State the blood parasite species.
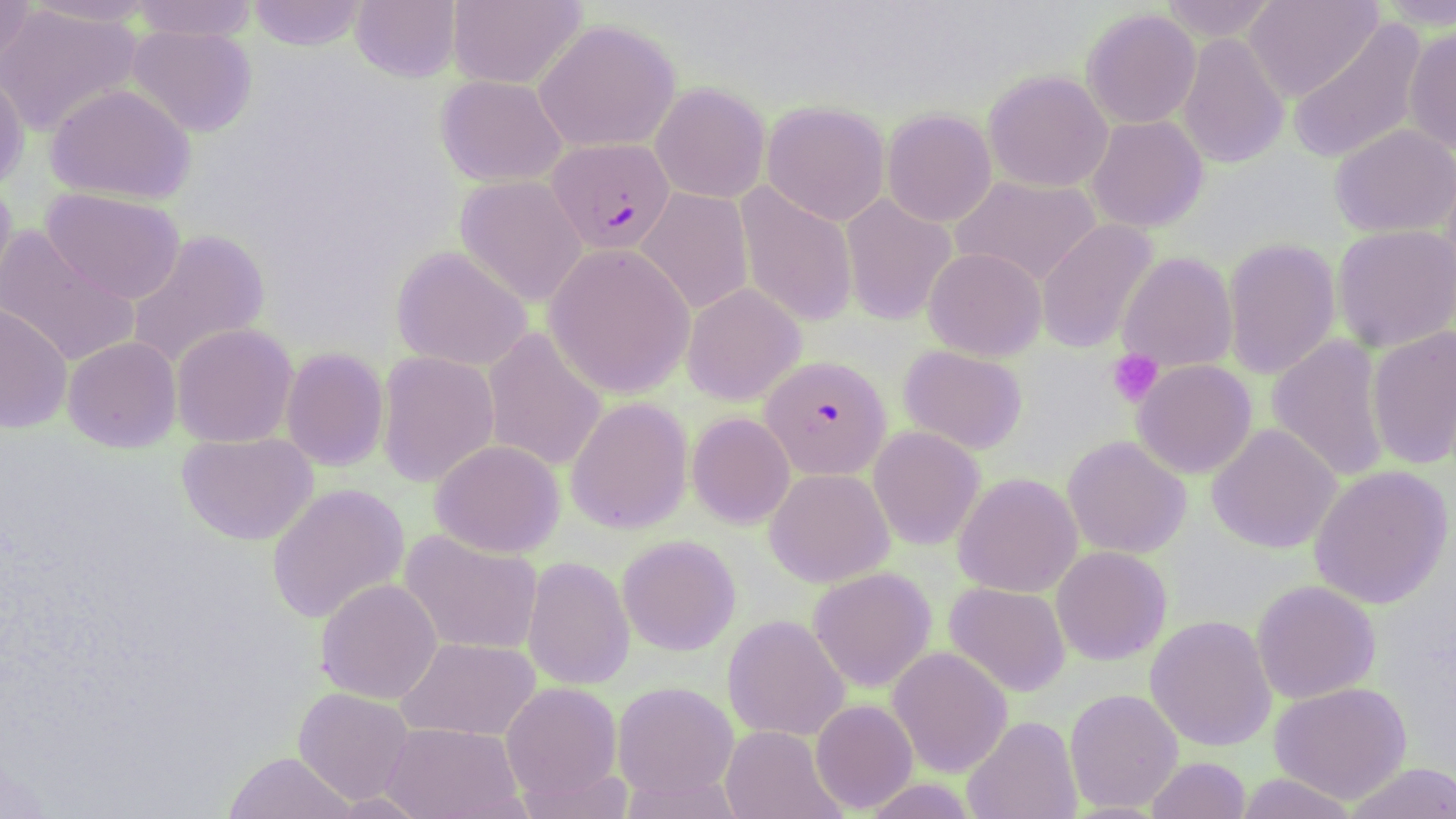
Plasmodium falciparum.

Approximate bounding boxes as [x1, y1, x2, y2] in pixels. Uninfected red blood cell locations: [0, 0, 35, 75], [22, 0, 161, 26], [130, 0, 258, 41], [248, 0, 367, 50], [351, 0, 461, 82], [447, 0, 586, 89], [1158, 0, 1280, 41], [1242, 0, 1381, 101], [1374, 0, 1456, 31], [0, 4, 143, 137], [1081, 7, 1201, 129], [1288, 17, 1428, 165], [533, 18, 681, 153], [126, 24, 258, 137], [1403, 26, 1456, 155], [1176, 32, 1290, 169], [0, 68, 29, 191], [983, 70, 1113, 192], [435, 75, 567, 187], [650, 82, 770, 203], [45, 83, 196, 204], [761, 100, 890, 226], [882, 109, 997, 227], [1086, 115, 1208, 233], [1330, 124, 1456, 238], [1439, 167, 1456, 298], [455, 175, 588, 307], [950, 175, 1102, 287], [0, 176, 17, 306], [734, 183, 859, 328], [41, 188, 186, 304], [635, 188, 754, 315], [840, 194, 957, 326], [1036, 219, 1158, 354], [1332, 224, 1456, 353], [0, 225, 141, 368], [125, 229, 270, 369], [1222, 237, 1341, 380], [544, 243, 695, 399], [391, 246, 533, 372], [923, 247, 1046, 361], [1118, 252, 1237, 372], [682, 283, 806, 406], [0, 302, 72, 434], [171, 323, 298, 448], [1366, 326, 1456, 470], [482, 327, 608, 472], [1267, 335, 1391, 482], [63, 336, 182, 453], [898, 345, 1028, 455], [280, 347, 390, 471], [376, 351, 500, 487], [1132, 359, 1257, 479], [565, 397, 693, 534], [687, 412, 795, 528], [1206, 423, 1342, 554], [867, 425, 985, 551], [177, 431, 318, 545], [1062, 435, 1191, 558], [430, 440, 565, 558], [1308, 465, 1454, 609], [764, 467, 894, 587], [953, 472, 1082, 597], [266, 483, 409, 624], [399, 529, 543, 656], [617, 535, 741, 655], [1051, 545, 1172, 665], [522, 556, 634, 691], [808, 567, 936, 693], [315, 578, 442, 704], [1251, 580, 1381, 704], [944, 581, 1070, 696], [723, 614, 850, 742], [1145, 615, 1276, 751], [396, 637, 541, 741], [887, 646, 1013, 777], [500, 681, 622, 804], [612, 681, 739, 799], [1269, 681, 1413, 804], [293, 687, 414, 805], [1064, 688, 1183, 812], [810, 699, 918, 813], [963, 715, 1082, 819], [382, 722, 523, 819], [720, 725, 845, 819], [223, 751, 356, 819], [1146, 756, 1251, 819], [1344, 762, 1456, 818], [1233, 773, 1360, 818], [864, 777, 978, 819], [328, 792, 432, 818]. Platelet locations: [1107, 349, 1163, 406]. Plasmodium falciparum-infected red blood cell locations: [547, 137, 675, 254], [760, 355, 891, 480]. Image is 1456×819 pixels. Thin blood film. Optical microscopy. Captured at 1000x magnification. Single field of view. May-Grünwald-Giemsa-stained preparation.